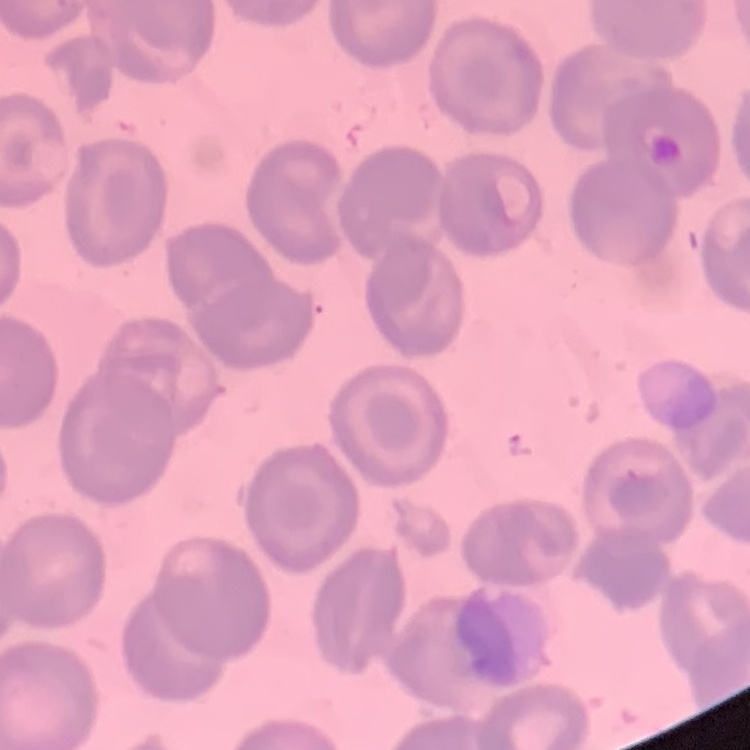

The erythrocytes show no rouleaux formation. Stained with either Field's or Giemsa. Thin blood smear. One tile cut from a larger photomicrograph.